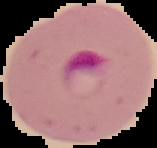

Summary:
  - Image size: 157×148 pixels
  - Result: Plasmodium parasites identified
  - Image type: segmented cell region on a black background
  - Preparation: thin blood film